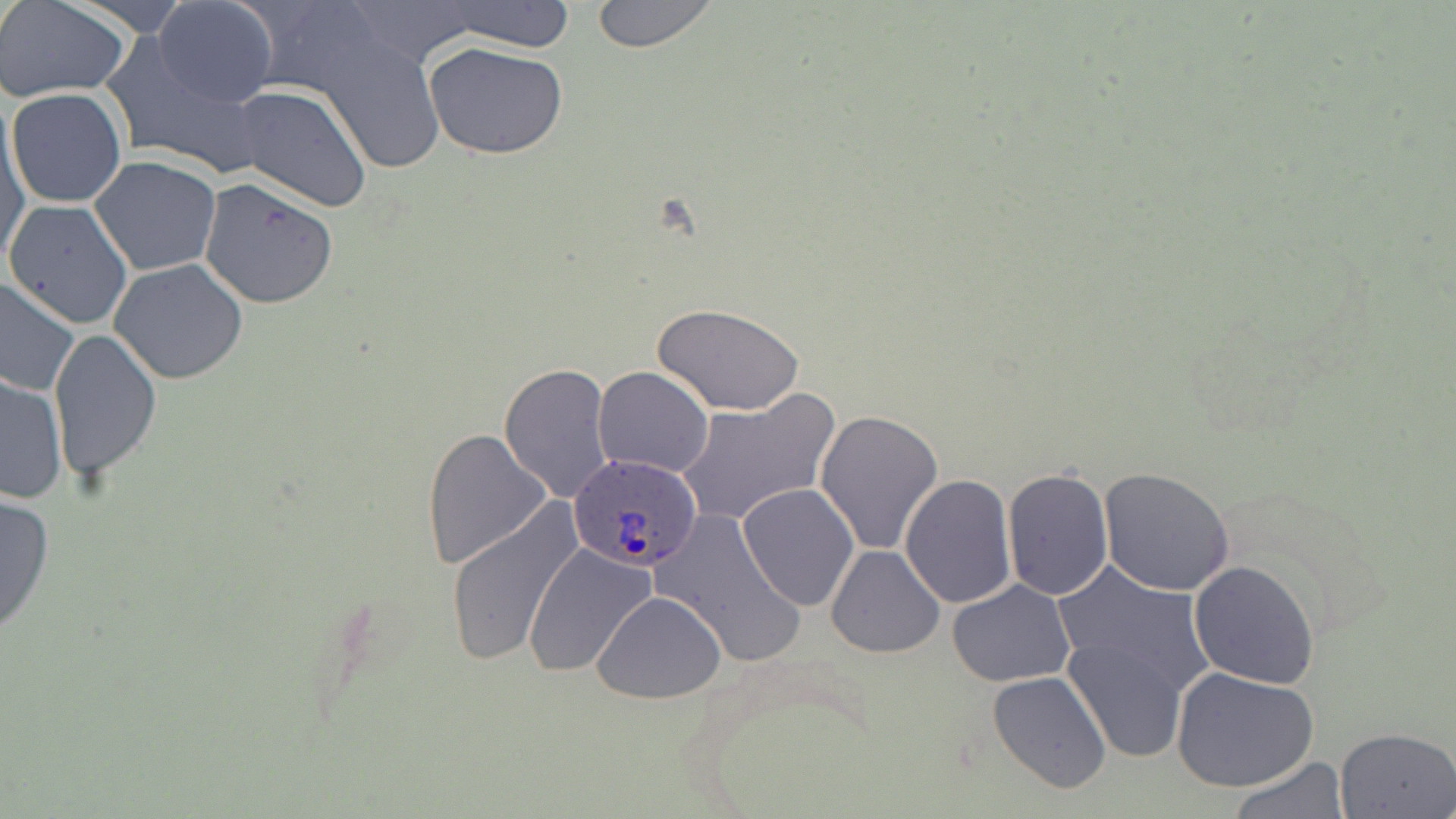
Approximate bounding boxes as (x1,y1)-(x2,y2) corner pairs in pixels. Plasmodium ovale-infected red blood cell locations: (567,453)-(703,571). Uninfected red blood cell locations: (154,0)-(278,108), (338,0)-(487,71), (590,0)-(718,52), (0,1)-(131,102), (430,1)-(579,52), (99,33)-(269,177), (319,35)-(446,173), (424,42)-(568,160), (233,84)-(372,213), (6,87)-(127,209), (1,109)-(30,266), (89,155)-(221,277), (198,179)-(339,309), (4,199)-(134,330), (110,259)-(249,386), (0,276)-(80,398), (652,303)-(805,417), (48,328)-(160,482), (498,363)-(613,502), (592,367)-(714,479), (0,372)-(66,505), (640,380)-(782,507), (676,392)-(840,529), (815,408)-(945,553), (422,430)-(551,570), (1099,467)-(1235,596), (1001,468)-(1114,601), (899,475)-(1016,609), (736,482)-(860,611), (0,492)-(54,636), (443,497)-(586,666), (657,510)-(803,668), (524,543)-(658,681), (825,543)-(945,659), (1188,561)-(1320,689), (1054,564)-(1216,700), (947,580)-(1075,688), (593,591)-(726,703), (1060,638)-(1186,765), (1173,667)-(1319,793), (987,670)-(1112,794), (1335,726)-(1456,817), (1227,756)-(1349,817). Slide-level diagnosis: Plasmodium ovale. Optical microscopy. 1000x magnification. May-Grünwald-Giemsa-stained preparation. Image is 1456×819 pixels. Thin blood smear. Single field of view.